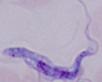

Summary:
  - Identification: trypanosome
  - Magnification: 1000x
  - Modality: micrograph